Identify the blood parasite species.
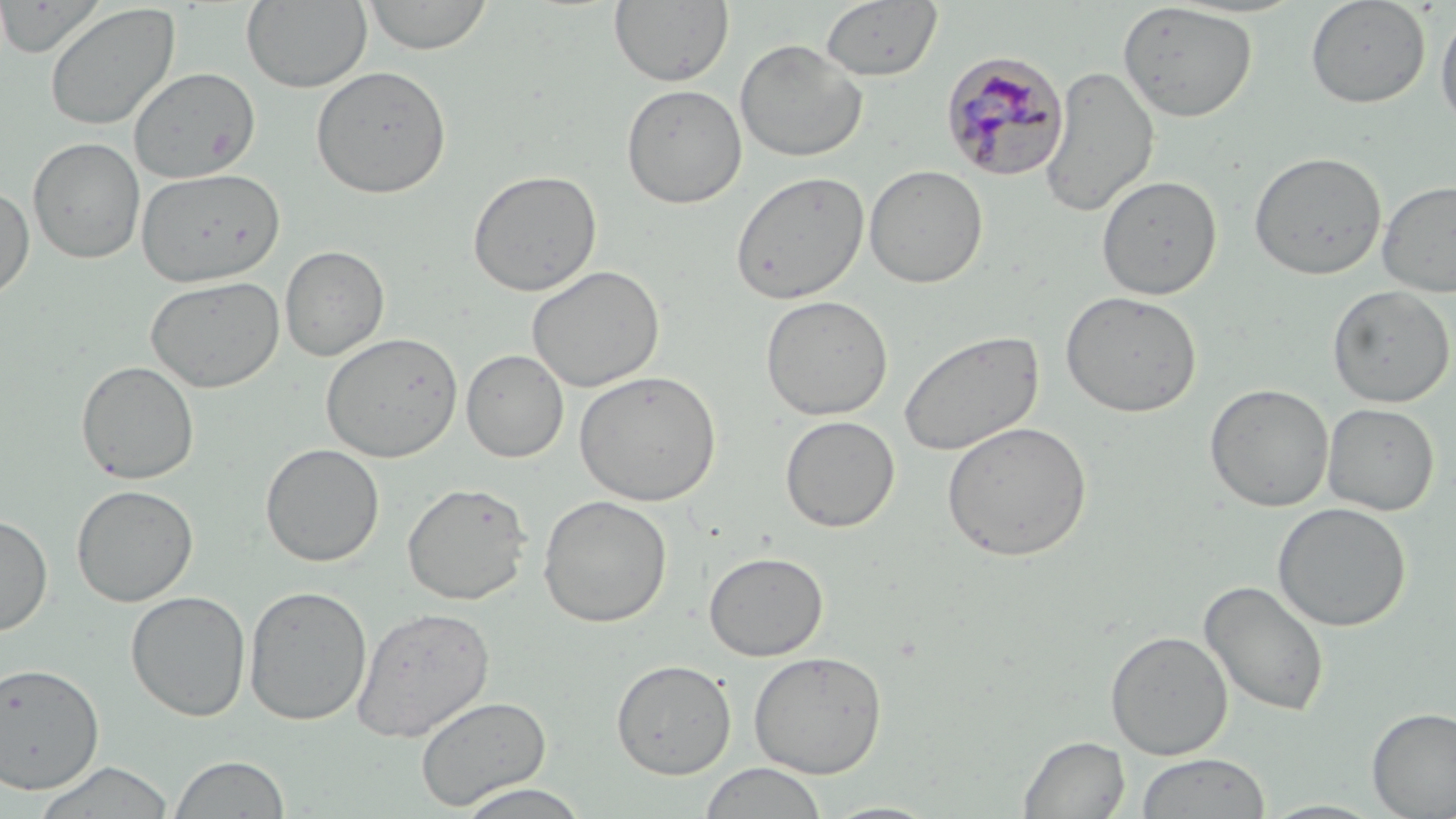

Plasmodium malariae.

Approximate bounding boxes as [x1, y1, x2, y2] in pixels. Plasmodium malariae-infected red blood cell locations: [940, 51, 1070, 182]. Uninfected red blood cell locations: [241, 0, 372, 93], [361, 0, 494, 55], [609, 0, 735, 88], [1305, 0, 1431, 108], [819, 1, 943, 82], [44, 2, 180, 132], [1117, 2, 1258, 123], [1435, 7, 1456, 133], [735, 38, 867, 162], [310, 65, 452, 199], [1040, 65, 1160, 217], [128, 67, 261, 182], [622, 84, 747, 209], [27, 137, 145, 265], [1248, 150, 1387, 280], [864, 165, 988, 288], [135, 167, 286, 287], [467, 168, 603, 297], [730, 170, 870, 305], [1096, 174, 1222, 300], [1377, 179, 1456, 297], [0, 185, 35, 302], [279, 245, 389, 361], [526, 265, 665, 392], [145, 275, 285, 393], [1327, 284, 1454, 408], [1061, 290, 1202, 418], [760, 295, 894, 420], [899, 328, 1044, 457], [320, 332, 463, 462], [461, 349, 569, 463], [76, 360, 200, 485], [573, 369, 722, 506], [1204, 383, 1334, 512], [1321, 402, 1440, 516], [780, 415, 900, 532], [942, 420, 1093, 561], [260, 443, 385, 567], [402, 481, 532, 605], [71, 484, 198, 607], [537, 494, 673, 628], [1272, 502, 1411, 632], [0, 513, 53, 636], [704, 550, 828, 661], [1199, 578, 1330, 717], [243, 584, 373, 726], [125, 590, 251, 721], [352, 605, 495, 741], [1105, 630, 1233, 760], [748, 650, 887, 778], [611, 659, 737, 779], [0, 661, 105, 794], [414, 695, 551, 811], [1366, 706, 1456, 817], [1018, 735, 1130, 818], [1135, 752, 1271, 818], [167, 754, 291, 818], [30, 760, 176, 818], [699, 762, 828, 819], [451, 783, 593, 819], [1257, 799, 1388, 818]. Thin blood smear. Optical microscopy. May-Grünwald-Giemsa-stained preparation. Image is 1456×819 pixels. One field of a larger specimen. Captured at 1000x magnification.